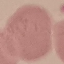

Malaria status: uninfected. Giemsa stain. Photographed with a smartphone camera at the microscope eyepiece. Thin blood smear. Automatically extracted cell patch, resized to 64 × 64 pixels.